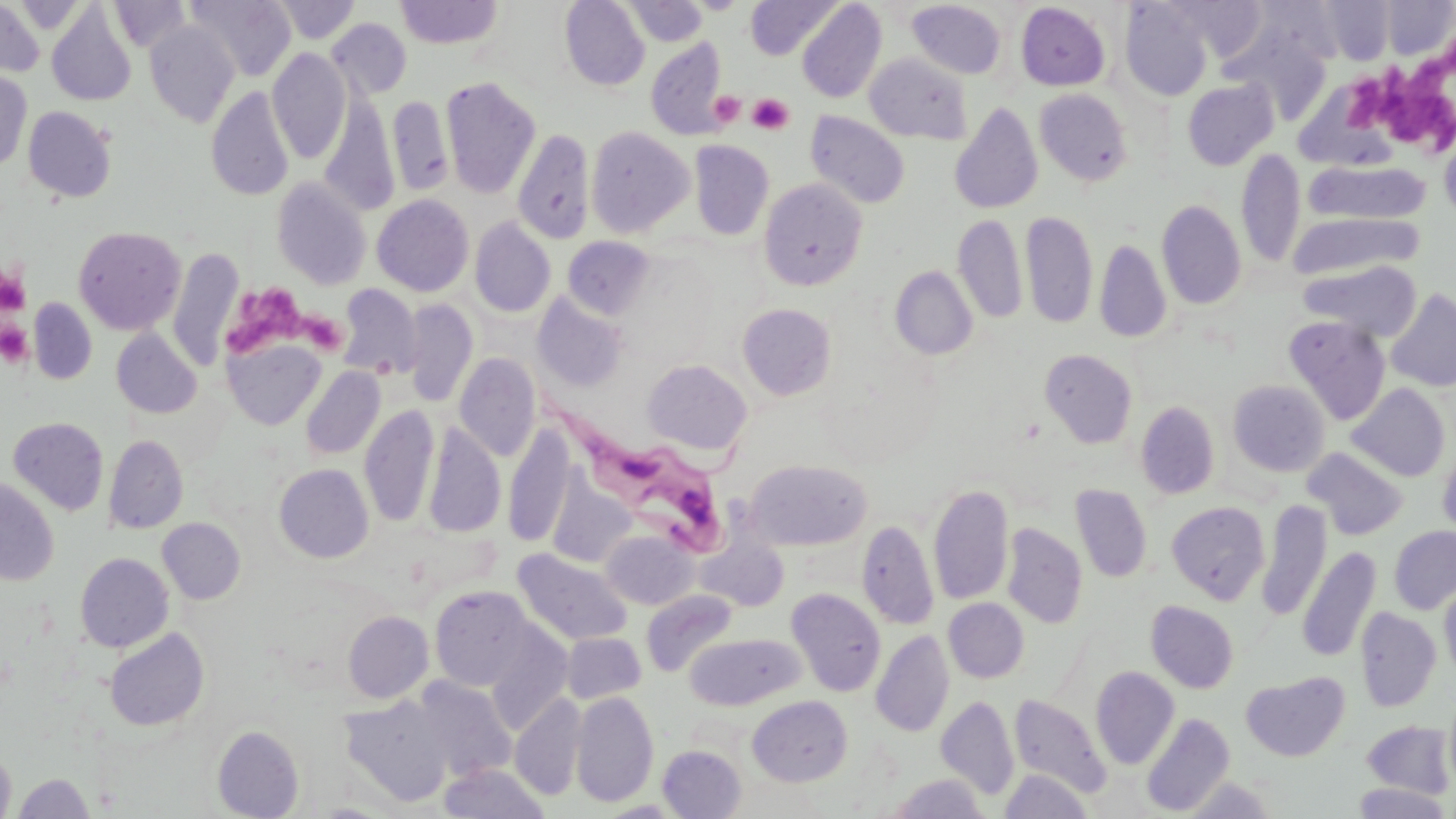

Summary:
  - Coordinate format: approximate bounding boxes as (x1, y1, x2, y2) in pixels
  - Platelet locations: (1413, 58, 1451, 97), (1341, 76, 1388, 129), (710, 91, 746, 127), (747, 93, 794, 135), (1388, 97, 1449, 147), (0, 266, 29, 315), (224, 282, 307, 358), (298, 311, 347, 355), (0, 321, 33, 367)
  - Trypanosoma brucei locations: (532, 395, 729, 564)
  - Uninfected red blood cell locations: (0, 0, 44, 78), (109, 0, 191, 53), (186, 0, 297, 82), (272, 0, 360, 44), (560, 0, 649, 90), (685, 0, 750, 14), (746, 0, 840, 59), (1380, 0, 1455, 59), (394, 1, 504, 49), (623, 1, 708, 46), (907, 1, 1007, 79), (1120, 1, 1213, 101), (1174, 1, 1268, 59), (1317, 1, 1395, 64), (796, 2, 886, 104), (1016, 3, 1110, 91), (47, 4, 136, 107), (327, 17, 411, 99), (144, 21, 240, 127), (1226, 30, 1332, 124), (646, 40, 728, 140), (267, 48, 350, 164), (865, 53, 972, 144), (0, 70, 32, 173), (441, 77, 541, 199), (1182, 79, 1278, 170), (206, 86, 294, 201), (1035, 88, 1133, 186), (320, 93, 399, 217), (387, 95, 453, 196), (949, 104, 1043, 214), (23, 106, 117, 203), (805, 110, 910, 209), (584, 126, 694, 238), (512, 129, 595, 245), (1439, 130, 1456, 226), (690, 140, 774, 240), (1236, 147, 1305, 270), (1304, 159, 1432, 227), (272, 177, 372, 290), (758, 177, 868, 291), (372, 194, 474, 297), (1156, 200, 1246, 310), (1020, 210, 1097, 329), (1290, 211, 1423, 280), (953, 213, 1027, 325), (470, 218, 556, 317), (73, 225, 186, 335), (562, 236, 655, 319), (1094, 238, 1172, 343), (168, 247, 243, 370), (1299, 259, 1422, 341), (890, 266, 978, 360), (337, 284, 423, 380), (1385, 288, 1456, 392), (533, 292, 629, 393), (28, 297, 97, 384), (402, 299, 478, 407), (737, 303, 837, 401), (1282, 316, 1391, 425), (111, 328, 202, 418), (224, 338, 325, 430), (1039, 349, 1137, 448), (454, 352, 541, 461), (642, 359, 752, 456), (301, 366, 385, 461), (1228, 380, 1330, 477), (1347, 383, 1451, 482), (1135, 401, 1219, 499), (359, 404, 439, 527), (8, 417, 109, 515), (423, 424, 505, 538), (503, 424, 575, 549), (104, 435, 188, 534), (1438, 443, 1456, 540), (1303, 448, 1408, 540), (745, 459, 871, 550), (274, 463, 374, 563), (0, 478, 59, 586), (546, 478, 637, 568), (928, 482, 1013, 606), (1071, 484, 1152, 582), (1257, 500, 1331, 621), (1166, 501, 1270, 603), (157, 518, 245, 604), (857, 518, 939, 630), (1002, 523, 1087, 628), (1389, 526, 1456, 614), (601, 530, 697, 610), (697, 536, 789, 612), (1298, 546, 1381, 662), (512, 548, 632, 646), (75, 552, 174, 652), (1440, 579, 1456, 684), (430, 585, 535, 690), (786, 588, 886, 696), (641, 591, 738, 678), (944, 598, 1029, 682), (1147, 601, 1239, 693), (1355, 608, 1442, 712), (343, 611, 434, 703), (484, 622, 574, 734), (104, 628, 209, 732), (871, 630, 954, 737), (562, 632, 646, 704), (686, 632, 804, 709), (1091, 667, 1179, 769), (1240, 671, 1350, 762), (413, 678, 516, 782), (571, 691, 659, 807), (510, 693, 587, 801), (338, 695, 456, 807), (747, 695, 852, 786), (1009, 695, 1111, 798), (936, 696, 1020, 801), (1142, 712, 1235, 816), (1361, 721, 1455, 798), (212, 726, 304, 818), (657, 745, 746, 818), (0, 748, 16, 819), (439, 763, 550, 819), (1000, 770, 1093, 818), (14, 773, 95, 818), (887, 774, 991, 818), (1180, 777, 1278, 818), (1350, 783, 1453, 818)
  - Slide-level diagnosis: Trypanosoma brucei
  - Field of view: single
  - Magnification: 1000x
  - Modality: light microscopy
  - Image size: 1456×819 pixels
  - Preparation: thin blood film
  - Stain: May-Grünwald-Giemsa